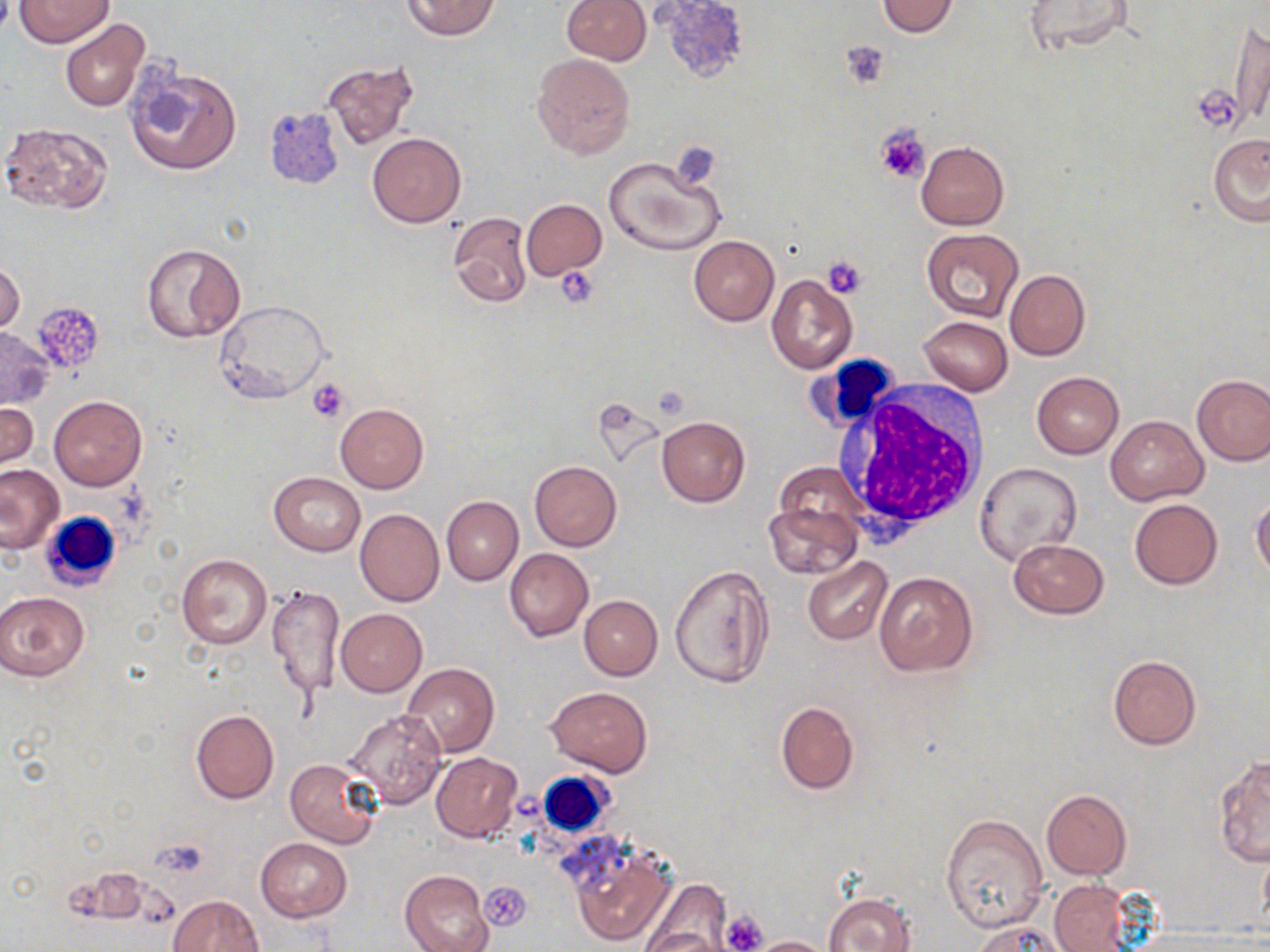

Summary:
  - Coordinate format: approximate bounding boxes as (x1, y1, x2, y2) in pixels
  - Uninfected red blood cell locations: (15, 0, 114, 46), (401, 0, 499, 42), (561, 0, 649, 65), (657, 0, 753, 83), (876, 1, 959, 37), (1023, 2, 1136, 55), (59, 19, 149, 113), (1231, 20, 1269, 130), (532, 53, 634, 158), (321, 60, 422, 152), (124, 61, 243, 178), (1, 120, 116, 214), (368, 133, 465, 228), (1207, 134, 1270, 226), (915, 141, 1009, 230), (603, 154, 727, 256), (521, 199, 606, 280), (447, 211, 532, 308), (921, 229, 1026, 323), (688, 236, 779, 326), (140, 242, 244, 343), (1, 259, 25, 337), (1005, 269, 1090, 360), (767, 274, 858, 375), (213, 300, 329, 403), (917, 316, 1013, 395), (1, 326, 54, 409), (1032, 372, 1124, 458), (1192, 372, 1270, 466), (49, 395, 147, 490), (1, 403, 39, 478), (335, 403, 429, 494), (1106, 415, 1208, 505), (657, 416, 749, 506), (529, 460, 621, 550), (975, 462, 1081, 567), (1, 465, 64, 552), (269, 471, 365, 555), (1251, 494, 1270, 581), (441, 496, 523, 586), (1129, 498, 1223, 590), (764, 500, 860, 579), (355, 508, 444, 606), (1007, 537, 1109, 619), (504, 548, 593, 641), (176, 554, 272, 649), (802, 555, 892, 645), (670, 563, 774, 688), (874, 571, 979, 678), (267, 585, 346, 700), (0, 592, 89, 680), (578, 595, 662, 680), (335, 609, 427, 696), (1108, 654, 1201, 749), (402, 662, 499, 757), (546, 687, 653, 776), (775, 700, 860, 795), (190, 710, 278, 804), (346, 710, 448, 808), (430, 752, 522, 842), (1214, 755, 1270, 866), (286, 758, 382, 849), (1041, 789, 1130, 879), (940, 811, 1047, 931), (255, 838, 353, 922), (568, 841, 676, 946), (402, 869, 494, 952), (641, 876, 736, 948), (1050, 879, 1134, 951), (824, 892, 915, 952), (168, 895, 264, 952), (972, 919, 1075, 951), (641, 928, 727, 951), (747, 935, 833, 952)
  - White blood cell locations: (807, 355, 905, 434), (828, 379, 993, 540), (38, 510, 122, 590), (536, 771, 614, 839)
  - Platelet locations: (840, 40, 892, 89), (1193, 85, 1244, 132), (874, 123, 930, 184), (668, 141, 722, 189), (822, 256, 869, 299), (556, 266, 599, 307), (31, 302, 106, 374), (307, 379, 351, 423), (481, 881, 532, 932), (719, 910, 768, 952)
  - Slide-level diagnosis: negative for blood parasites
  - Magnification: 1000x
  - Stain: May-Grünwald-Giemsa
  - Preparation: thin blood film
  - Image size: 1270×952 pixels
  - Field of view: single
  - Modality: optical microscopy